Evaluate for Plasmodium parasites.
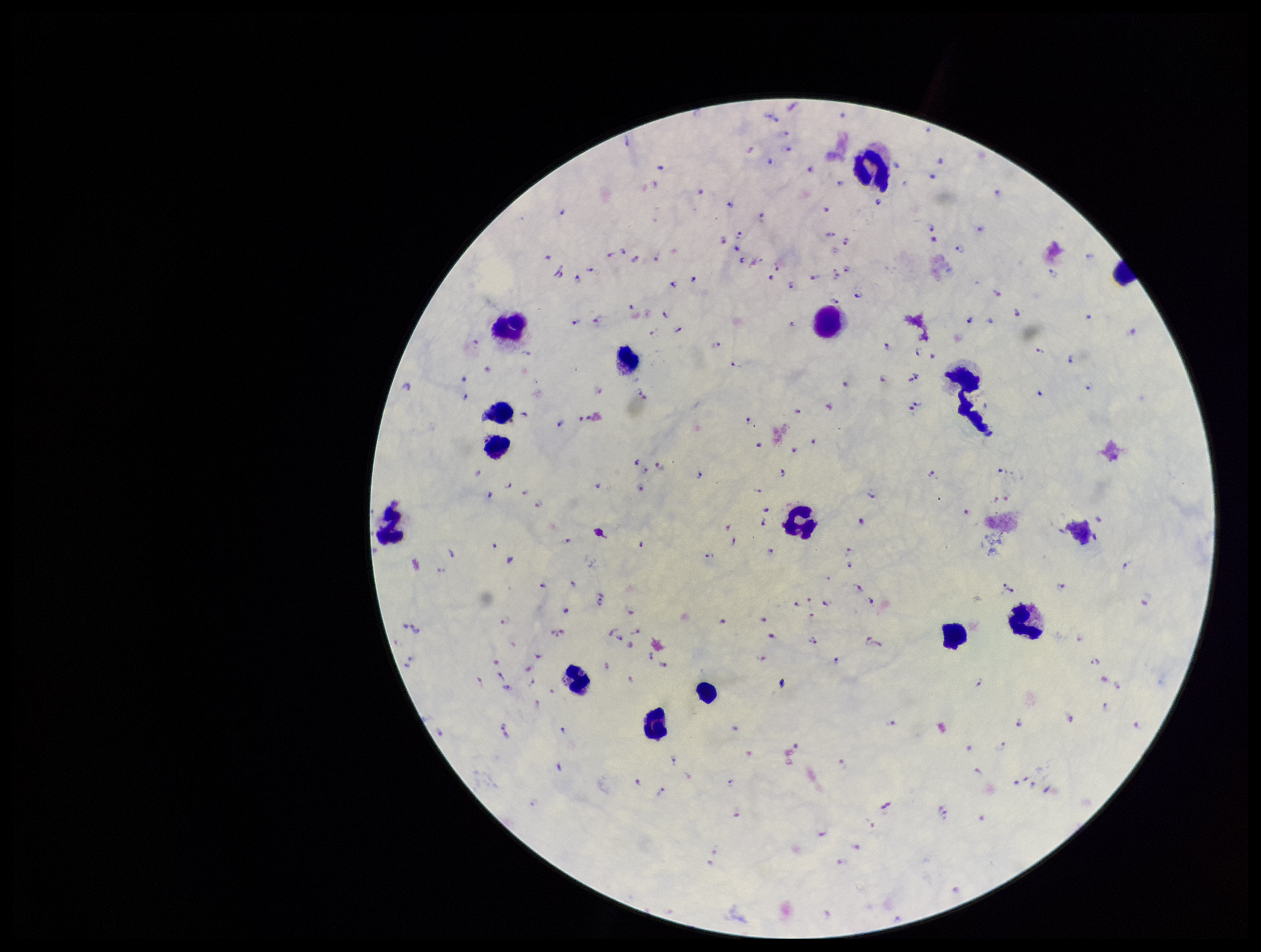

Identified.

Smartphone photograph taken through the eyepiece of a microscope. Patient malaria status: positive. Parasite count: 203. Species reported for this patient: Plasmodium falciparum. Single field of view. Stained with Giemsa. Leukocyte count: 15. Image is 1261×952 pixels. Preparation: thick.